Classify this cell by malaria status.
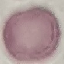

Uninfected.

Summary:
  - Preparation: thin blood film
  - Image type: cell patch, automatically extracted from a larger field of view and resized to 64 × 64 pixels
  - Stain: Giemsa
  - Capture: smartphone through the microscope eyepiece